Point out each leukocyte.
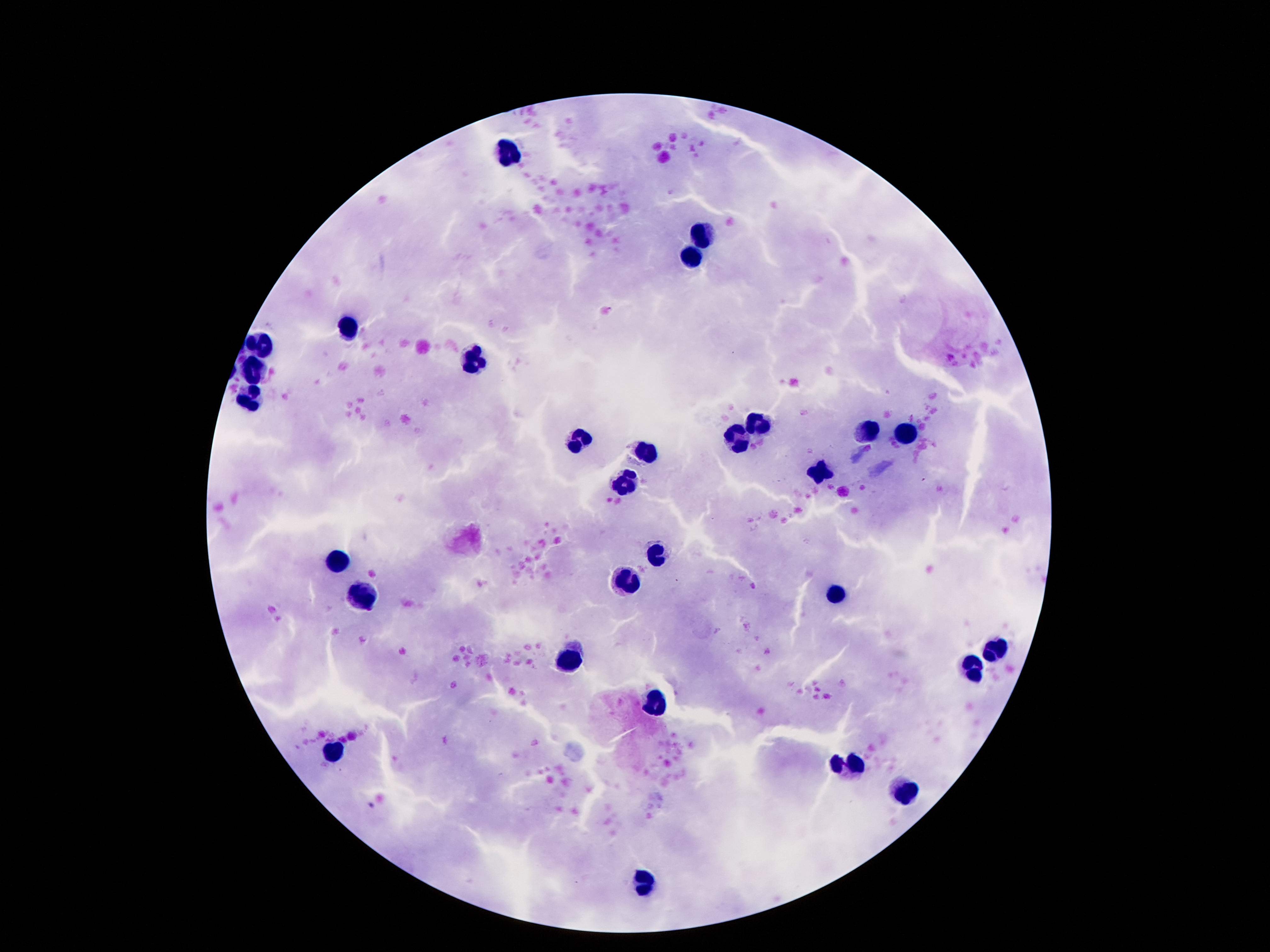
Approximate centers as [x, y] in pixels.
Leukocytes: [502, 150], [704, 234], [689, 251], [349, 330], [259, 346], [476, 358], [254, 367], [250, 400], [758, 426], [870, 430], [904, 435], [736, 439], [579, 441], [646, 452], [818, 469], [627, 483], [659, 555], [336, 559], [625, 585], [360, 595], [833, 595], [995, 649], [571, 662], [975, 668], [657, 703], [334, 752], [849, 763], [904, 792], [642, 881].

Photographed through the microscope eyepiece with a smartphone camera. One field from this slide. Thick blood smear. Patient malaria status: not infected. 100x magnification. Image is 1270×952 pixels. Giemsa-stained preparation.